Name the parasite shown.
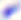

This is Toxoplasma gondii.

Micrograph. Captured at 400x magnification.